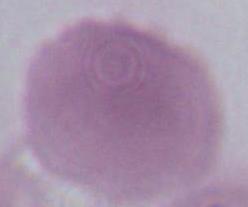

magnification = 1000x
identification = red blood cell
modality = photomicrograph